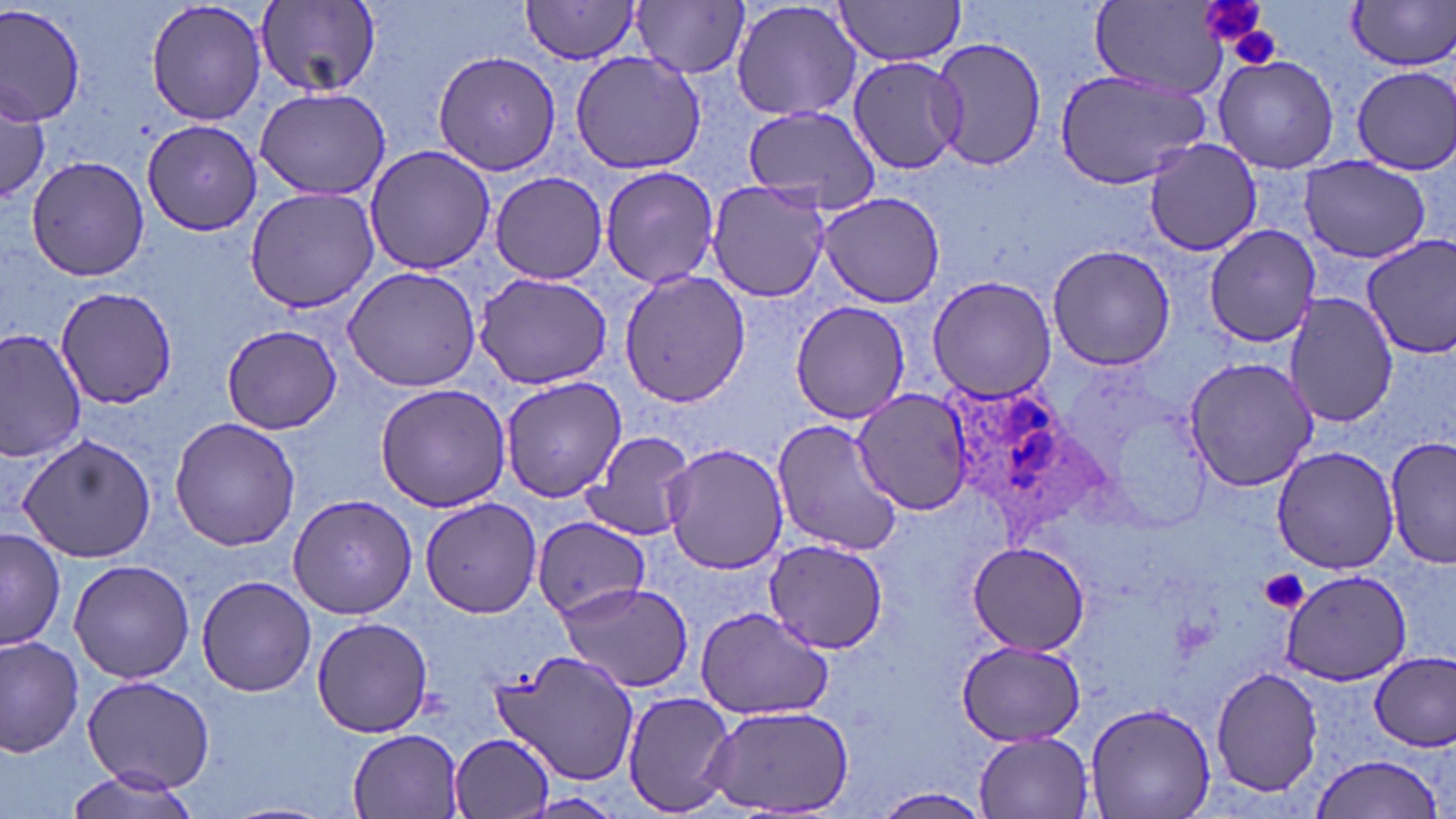
{
  "slide_level_diagnosis": "Plasmodium ovale",
  "image_size": "1456×819 pixels",
  "plasmodium_ovale_infected_red_blood_cell_locations": "approximate bounding boxes as (x1, y1, x2, y2) in pixels: (939, 378, 1105, 535)",
  "preparation": "thin blood film",
  "platelet_locations": "approximate bounding boxes as (x1, y1, x2, y2) in pixels: (1200, 0, 1271, 54), (1224, 21, 1285, 69), (1260, 570, 1309, 614)",
  "modality": "light microscopy",
  "stain": "May-Grünwald-Giemsa",
  "field_of_view": "single",
  "magnification": "1000x",
  "uninfected_red_blood_cell_locations": "approximate bounding boxes as (x1, y1, x2, y2) in pixels: (145, 0, 265, 127), (731, 0, 863, 123), (833, 0, 967, 66), (254, 1, 384, 96), (631, 1, 751, 79), (1346, 1, 1456, 73), (0, 2, 86, 125), (518, 2, 644, 63), (1087, 2, 1232, 96), (930, 37, 1050, 173), (569, 49, 709, 175), (431, 50, 563, 176), (1212, 55, 1340, 173), (845, 56, 966, 174), (1351, 64, 1455, 172), (1054, 69, 1212, 191), (0, 86, 50, 199), (254, 86, 391, 202), (738, 105, 884, 216), (142, 120, 263, 238), (1141, 139, 1265, 256), (362, 144, 494, 276), (24, 155, 151, 283), (1301, 157, 1431, 263), (599, 164, 720, 290), (488, 172, 611, 282), (705, 180, 833, 303), (244, 187, 379, 316), (817, 193, 946, 308), (1202, 225, 1323, 348), (1360, 237, 1456, 358), (1046, 244, 1176, 371), (341, 264, 482, 393), (618, 268, 750, 410), (472, 271, 615, 390), (925, 274, 1058, 402), (57, 284, 179, 408), (1283, 291, 1397, 429), (788, 300, 911, 425), (222, 324, 342, 435), (0, 328, 87, 461), (1183, 355, 1319, 492), (500, 375, 627, 503), (376, 383, 512, 512), (850, 389, 976, 514), (169, 416, 300, 551), (771, 419, 904, 558), (579, 430, 698, 540), (13, 432, 157, 562), (1385, 439, 1455, 570), (662, 441, 789, 575), (1271, 444, 1399, 574), (287, 494, 416, 619), (420, 498, 543, 618), (531, 517, 651, 619), (1, 527, 65, 653), (764, 539, 889, 654), (965, 542, 1091, 656), (67, 559, 198, 685), (1276, 570, 1414, 685), (196, 575, 318, 697), (556, 581, 696, 690), (695, 607, 834, 719), (312, 615, 434, 738), (0, 633, 84, 756), (955, 641, 1089, 746), (492, 646, 641, 785), (1370, 651, 1455, 752), (1210, 667, 1322, 796), (81, 676, 214, 792), (622, 689, 736, 816), (1085, 700, 1215, 819), (700, 703, 858, 816), (346, 728, 468, 819), (973, 731, 1096, 817), (450, 734, 557, 819), (1309, 753, 1445, 819), (61, 767, 207, 819), (868, 788, 993, 819)"
}